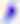

Toxoplasma gondii is seen. 400x magnification. Photomicrograph.